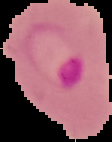
{
  "image_type": "cell region segmented out of the field of view; surrounding area masked to black",
  "image_size": "112×142 pixels",
  "malaria_status": "parasitized",
  "preparation": "thin blood smear"
}